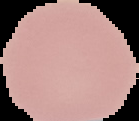 Malaria status: uninfected. Cell region segmented out of the field of view; the surrounding area is masked to black. Image is 139×121 pixels. From a thin blood film.